Give the extent of all Plasmodium falciparum-infected red blood cells.
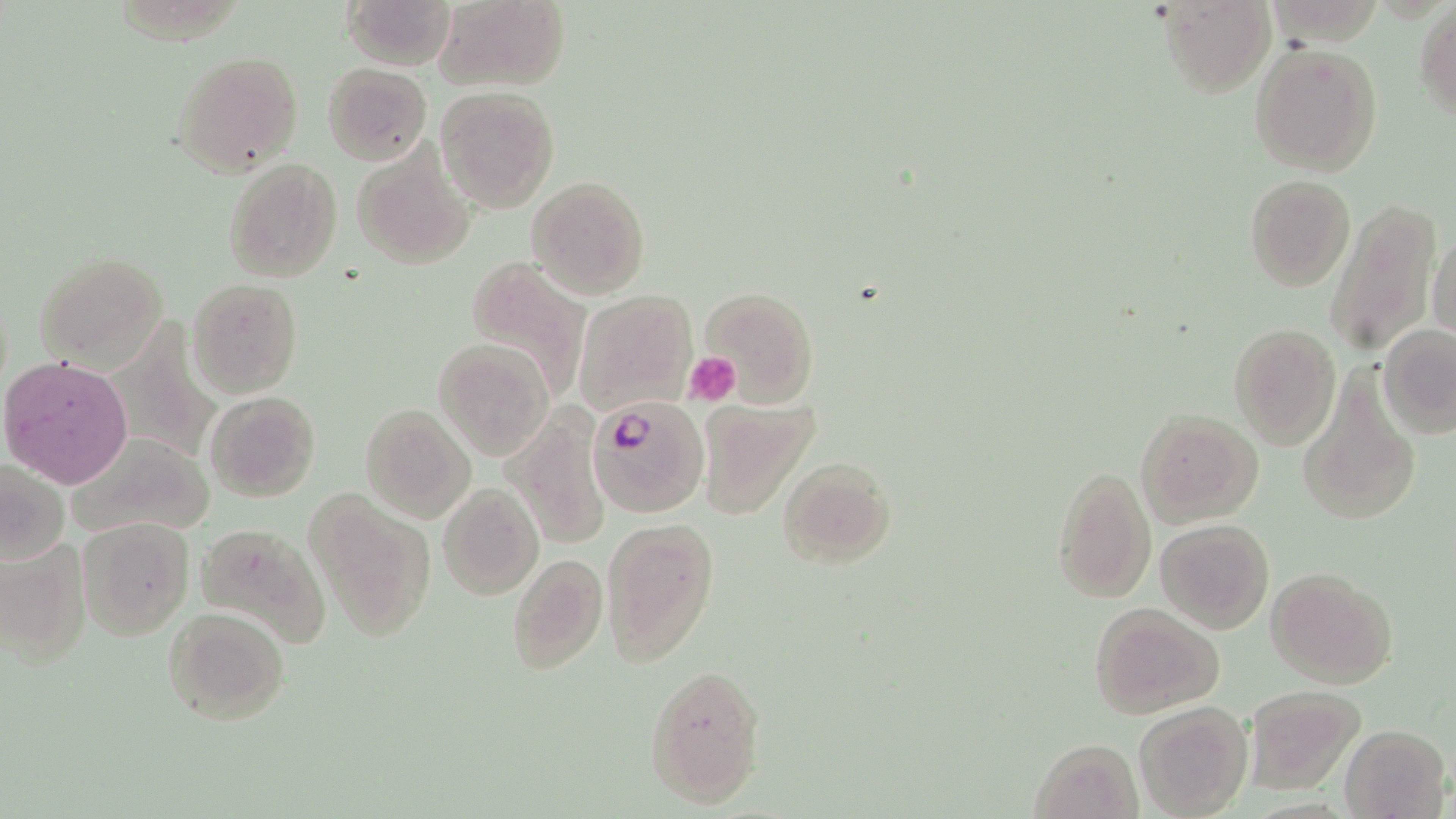

Approximate bounding boxes as named x1/y1/x2/y2 corners in pixels.
Plasmodium falciparum-infected red blood cells: (x1=589, y1=392, x2=710, y2=517).

Summary:
  - Uninfected red blood cell locations: (x1=341, y1=0, x2=454, y2=70), (x1=432, y1=0, x2=570, y2=95), (x1=1158, y1=1, x2=1276, y2=95), (x1=1415, y1=6, x2=1456, y2=121), (x1=1249, y1=40, x2=1383, y2=177), (x1=171, y1=50, x2=304, y2=179), (x1=322, y1=62, x2=431, y2=164), (x1=436, y1=87, x2=560, y2=213), (x1=353, y1=146, x2=475, y2=271), (x1=223, y1=158, x2=342, y2=283), (x1=1244, y1=175, x2=1355, y2=290), (x1=526, y1=176, x2=652, y2=299), (x1=1323, y1=197, x2=1443, y2=357), (x1=1428, y1=231, x2=1455, y2=342), (x1=34, y1=251, x2=169, y2=371), (x1=465, y1=253, x2=593, y2=402), (x1=188, y1=278, x2=302, y2=397), (x1=700, y1=286, x2=818, y2=405), (x1=574, y1=291, x2=697, y2=417), (x1=1230, y1=323, x2=1340, y2=447), (x1=1379, y1=325, x2=1456, y2=438), (x1=434, y1=336, x2=556, y2=461), (x1=1, y1=352, x2=135, y2=488), (x1=1298, y1=366, x2=1420, y2=529), (x1=206, y1=390, x2=321, y2=501), (x1=696, y1=399, x2=818, y2=520), (x1=361, y1=403, x2=474, y2=522), (x1=505, y1=408, x2=610, y2=549), (x1=1135, y1=408, x2=1264, y2=527), (x1=66, y1=433, x2=213, y2=539), (x1=0, y1=455, x2=67, y2=565), (x1=777, y1=456, x2=896, y2=570), (x1=1052, y1=465, x2=1156, y2=603), (x1=438, y1=482, x2=544, y2=600), (x1=310, y1=489, x2=435, y2=643), (x1=601, y1=516, x2=719, y2=667), (x1=77, y1=517, x2=193, y2=640), (x1=1155, y1=519, x2=1273, y2=634), (x1=194, y1=522, x2=332, y2=651), (x1=0, y1=538, x2=90, y2=672), (x1=506, y1=551, x2=607, y2=676), (x1=1266, y1=567, x2=1398, y2=688), (x1=1088, y1=602, x2=1222, y2=719), (x1=162, y1=606, x2=291, y2=725), (x1=645, y1=668, x2=766, y2=807), (x1=1244, y1=685, x2=1365, y2=793), (x1=1132, y1=702, x2=1253, y2=818), (x1=1341, y1=724, x2=1450, y2=818), (x1=1032, y1=737, x2=1142, y2=818)
  - Platelet locations: (x1=683, y1=352, x2=742, y2=406)
  - Slide-level diagnosis: Plasmodium falciparum
  - Modality: light microscopy
  - Magnification: 1000x
  - Image size: 1456×819 pixels
  - Stain: May-Grünwald-Giemsa
  - Field of view: single
  - Preparation: thin blood film